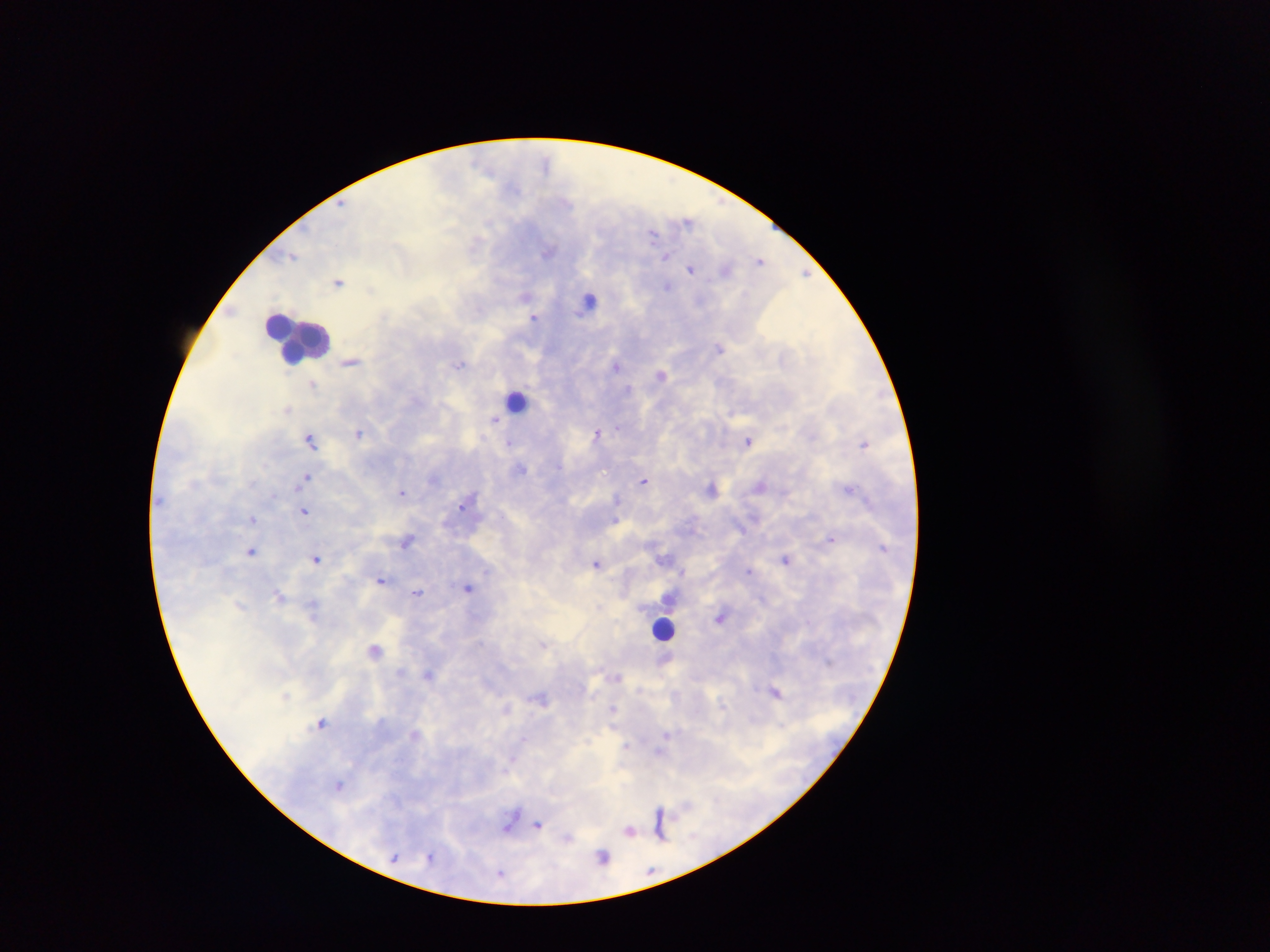
Approximate centers as (x, y) in pixels.
Summary:
  - Leukocyte locations: (589, 300), (297, 337), (515, 400), (663, 628), (510, 819)
  - Malaria parasite locations: (546, 161), (342, 204), (688, 221), (489, 224), (652, 234), (548, 251), (292, 256), (666, 257), (760, 261), (690, 268), (726, 270), (806, 273), (338, 282), (667, 286), (371, 288), (526, 295), (534, 317), (720, 348), (351, 361), (459, 364), (616, 366), (661, 374), (313, 385), (628, 389), (287, 409), (494, 419), (618, 427), (359, 432), (596, 433), (311, 439), (748, 440), (509, 442), (865, 443), (521, 468), (305, 477), (434, 479), (643, 480), (760, 485), (712, 488), (850, 488), (402, 493), (617, 499), (464, 503), (304, 511), (253, 519), (615, 521), (831, 538), (407, 541), (251, 551), (666, 558), (316, 559), (785, 559), (596, 563), (487, 571), (748, 571), (683, 573), (381, 580), (467, 588), (418, 592), (279, 594), (669, 598), (598, 607), (720, 617), (543, 644), (375, 649), (400, 671), (428, 674), (618, 677), (777, 693), (542, 698), (507, 708), (613, 709), (322, 722), (414, 733), (666, 734), (523, 739), (627, 745), (660, 750), (512, 759), (339, 785), (660, 813), (539, 825), (661, 825), (630, 830), (430, 855), (602, 856), (394, 858), (500, 874)
  - Image size: 1270×952 pixels
  - Field of view: single
  - Preparation: thick blood film
  - Country: Ghana
  - Capture: mobile-phone photograph through a microscope